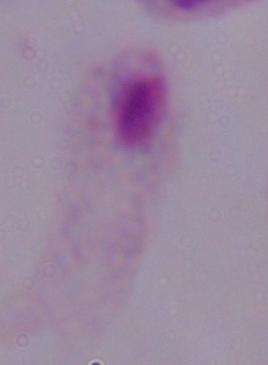
Micrograph. 1000x magnification. A trichomonad is seen.